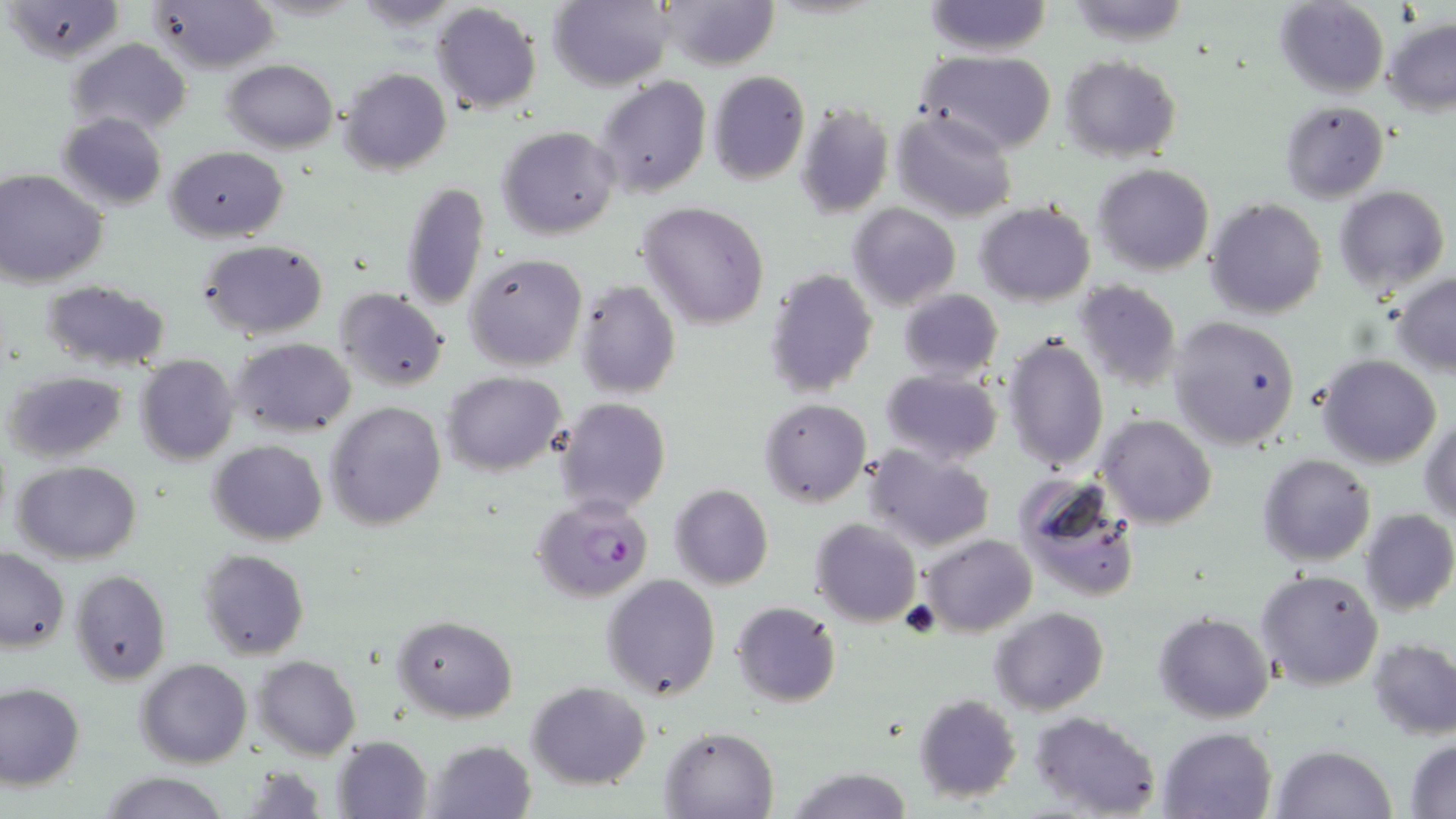
Summary:
  - Coordinate format: approximate bounding boxes as named x1/y1/x2/y2 corners in pixels
  - Uninfected red blood cell locations: (x1=5, y1=0, x2=126, y2=63), (x1=146, y1=0, x2=279, y2=74), (x1=550, y1=0, x2=673, y2=91), (x1=658, y1=0, x2=777, y2=70), (x1=923, y1=0, x2=1052, y2=56), (x1=1274, y1=0, x2=1390, y2=100), (x1=1063, y1=1, x2=1190, y2=45), (x1=430, y1=2, x2=541, y2=117), (x1=1382, y1=19, x2=1456, y2=115), (x1=68, y1=38, x2=191, y2=139), (x1=915, y1=50, x2=1059, y2=156), (x1=1059, y1=55, x2=1180, y2=162), (x1=223, y1=58, x2=338, y2=154), (x1=340, y1=69, x2=451, y2=175), (x1=707, y1=70, x2=810, y2=183), (x1=594, y1=75, x2=712, y2=199), (x1=537, y1=101, x2=686, y2=228), (x1=1279, y1=101, x2=1389, y2=203), (x1=796, y1=103, x2=894, y2=219), (x1=891, y1=108, x2=1018, y2=222), (x1=57, y1=111, x2=168, y2=212), (x1=497, y1=126, x2=619, y2=239), (x1=168, y1=147, x2=288, y2=240), (x1=1093, y1=163, x2=1214, y2=275), (x1=0, y1=169, x2=107, y2=286), (x1=398, y1=181, x2=490, y2=313), (x1=1334, y1=184, x2=1450, y2=294), (x1=1204, y1=198, x2=1328, y2=319), (x1=638, y1=201, x2=770, y2=329), (x1=975, y1=202, x2=1095, y2=306), (x1=847, y1=203, x2=960, y2=310), (x1=200, y1=239, x2=329, y2=340), (x1=465, y1=252, x2=587, y2=372), (x1=764, y1=268, x2=878, y2=398), (x1=1392, y1=273, x2=1456, y2=376), (x1=41, y1=280, x2=171, y2=372), (x1=574, y1=280, x2=681, y2=400), (x1=1074, y1=280, x2=1182, y2=388), (x1=335, y1=288, x2=449, y2=393), (x1=898, y1=288, x2=1004, y2=383), (x1=1166, y1=315, x2=1301, y2=450), (x1=1004, y1=332, x2=1109, y2=472), (x1=231, y1=337, x2=357, y2=436), (x1=135, y1=355, x2=239, y2=464), (x1=1316, y1=355, x2=1443, y2=468), (x1=4, y1=370, x2=128, y2=462), (x1=880, y1=370, x2=1003, y2=465), (x1=443, y1=371, x2=566, y2=476), (x1=553, y1=398, x2=671, y2=516), (x1=759, y1=398, x2=870, y2=507), (x1=326, y1=401, x2=446, y2=531), (x1=1095, y1=413, x2=1216, y2=528), (x1=1419, y1=417, x2=1455, y2=524), (x1=207, y1=440, x2=329, y2=544), (x1=863, y1=446, x2=993, y2=553), (x1=1258, y1=454, x2=1376, y2=565), (x1=12, y1=459, x2=143, y2=564), (x1=1015, y1=476, x2=1143, y2=606), (x1=669, y1=483, x2=774, y2=589), (x1=1359, y1=508, x2=1456, y2=617), (x1=811, y1=519, x2=921, y2=627), (x1=919, y1=535, x2=1037, y2=636), (x1=0, y1=548, x2=70, y2=652), (x1=198, y1=549, x2=310, y2=661), (x1=1253, y1=568, x2=1385, y2=692), (x1=72, y1=570, x2=170, y2=683), (x1=601, y1=575, x2=720, y2=701), (x1=731, y1=600, x2=841, y2=708), (x1=990, y1=606, x2=1109, y2=714), (x1=1153, y1=612, x2=1276, y2=723), (x1=393, y1=614, x2=516, y2=721), (x1=1369, y1=637, x2=1456, y2=739), (x1=254, y1=655, x2=360, y2=760), (x1=136, y1=659, x2=250, y2=767), (x1=0, y1=682, x2=85, y2=790), (x1=528, y1=682, x2=650, y2=788), (x1=914, y1=693, x2=1022, y2=803), (x1=1031, y1=711, x2=1162, y2=819), (x1=660, y1=725, x2=779, y2=819), (x1=1157, y1=727, x2=1277, y2=818), (x1=332, y1=735, x2=434, y2=819), (x1=426, y1=738, x2=537, y2=819), (x1=1406, y1=738, x2=1456, y2=817), (x1=1271, y1=744, x2=1396, y2=819), (x1=784, y1=766, x2=916, y2=819), (x1=101, y1=772, x2=232, y2=818)
  - Plasmodium falciparum-infected red blood cell locations: (x1=530, y1=495, x2=654, y2=603)
  - Slide-level diagnosis: Plasmodium falciparum
  - Magnification: 1000x
  - Stain: May-Grünwald-Giemsa
  - Modality: optical microscopy
  - Preparation: thin blood smear
  - Field of view: single
  - Image size: 1456×819 pixels